Comment on the morphology of the erythrocytes.
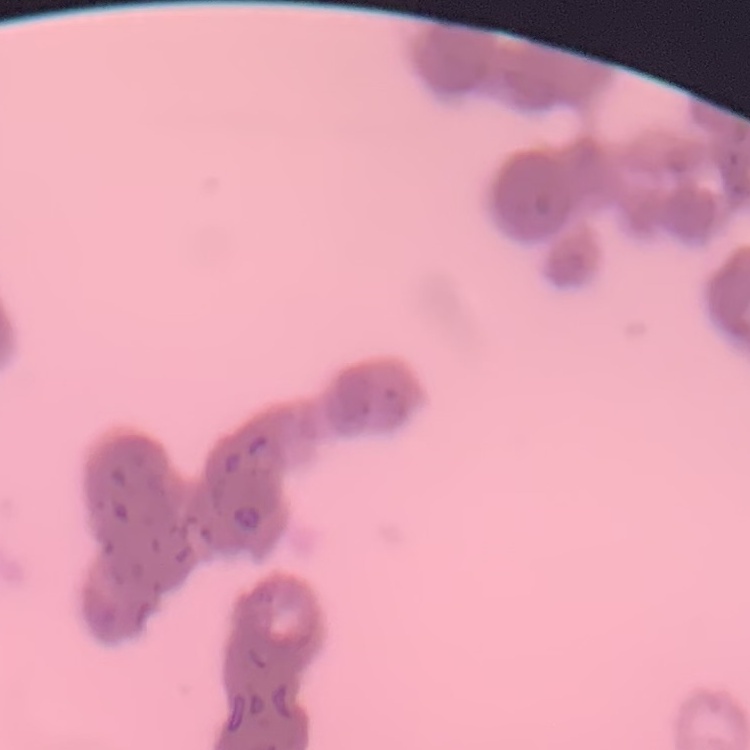
Rouleaux formation.

Thin blood film. Field's or Giemsa stain. Square crop of a larger photomicrograph.